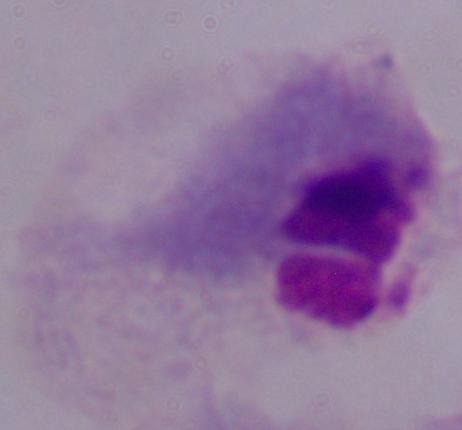

identification = trichomonad
modality = photomicrograph
magnification = 1000x